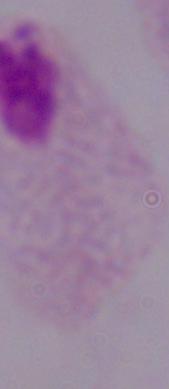
Summary:
  - Magnification: 1000x
  - Modality: micrograph
  - Identification: trichomonad